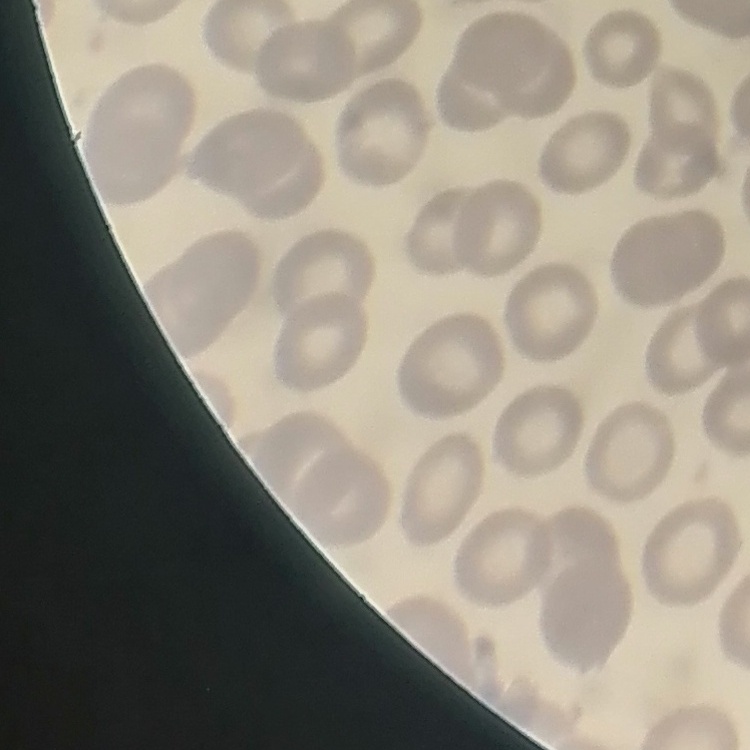
The erythrocytes show no rouleaux formation. Field's or Giemsa stain. One tile cut from a larger photomicrograph. Thin blood smear.